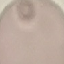

Malaria status: uninfected. Acquired by smartphone through the microscope eyepiece. Giemsa stain. Thin blood smear. Automatically extracted cell patch, resized to 64 × 64 pixels.